Name the parasite shown.
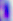
Toxoplasma gondii.

magnification = 400x
modality = photomicrograph